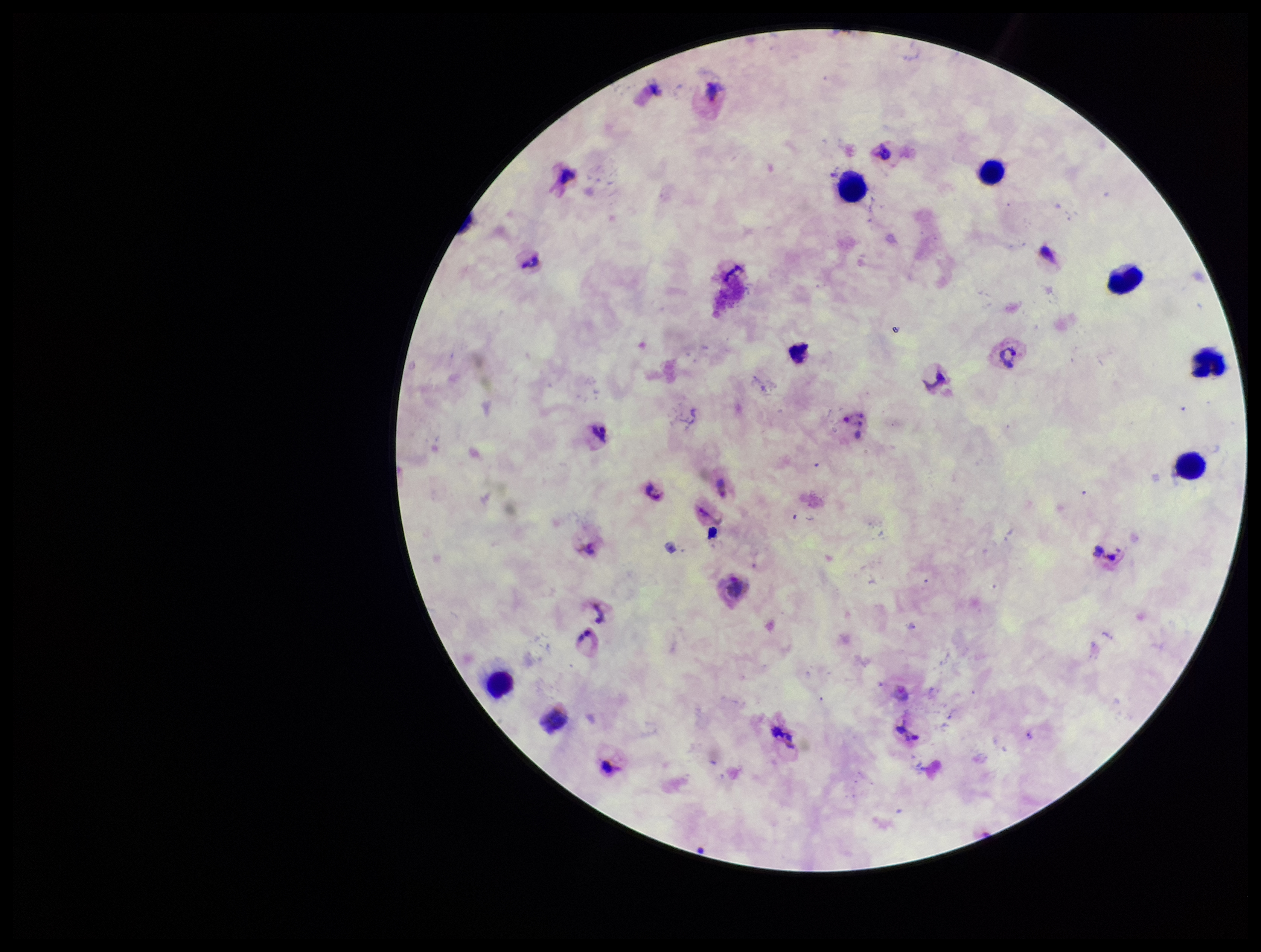

Summary:
  - Image size: 1261×952 pixels
  - Patient malaria status: infected
  - Species reported for this patient: Plasmodium vivax
  - Stain: Giemsa
  - Leukocyte count: 7
  - Preparation: thick smear
  - Parasite count: 4
  - Capture: smartphone photograph through the microscope eyepiece
  - Plasmodium parasites: detected
  - Field of view: one from this slide